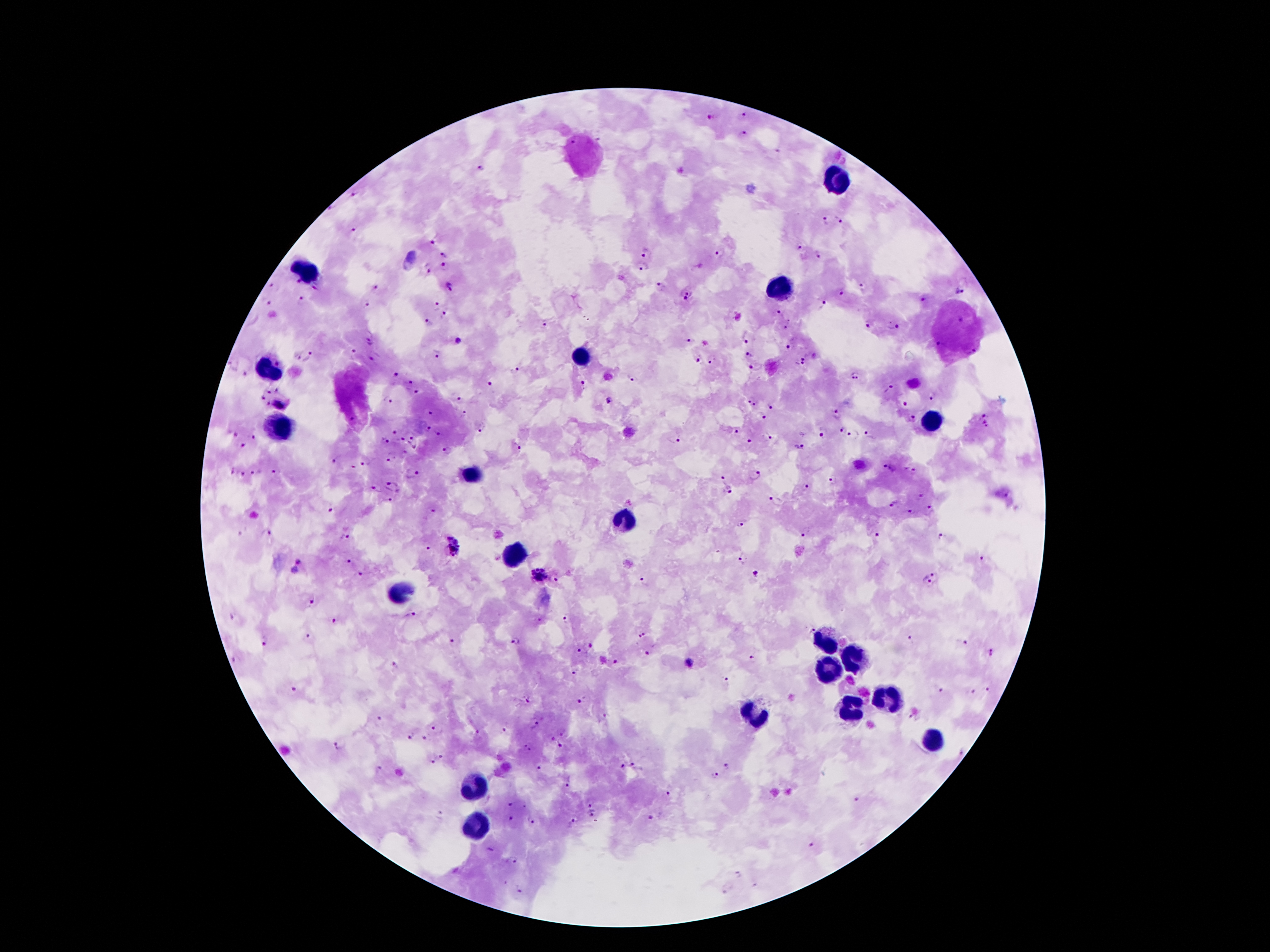

Approximate centers as [x, y] in pixels.
Summary:
  - Malaria parasite locations: [745, 114], [712, 117], [742, 135], [480, 168], [355, 196], [329, 210], [840, 219], [825, 221], [355, 230], [432, 241], [798, 247], [446, 253], [648, 253], [721, 253], [819, 256], [444, 266], [430, 267], [642, 267], [297, 281], [272, 287], [317, 287], [451, 287], [659, 287], [376, 288], [862, 288], [959, 292], [842, 293], [686, 296], [301, 299], [923, 300], [269, 302], [367, 303], [822, 304], [436, 305], [779, 313], [444, 314], [429, 323], [544, 325], [867, 325], [896, 327], [783, 328], [747, 337], [458, 340], [689, 340], [370, 341], [937, 345], [789, 346], [354, 350], [438, 351], [748, 355], [805, 356], [307, 357], [697, 359], [369, 360], [713, 360], [232, 364], [755, 366], [799, 366], [516, 370], [245, 375], [394, 375], [855, 375], [632, 378], [412, 380], [491, 382], [582, 383], [278, 388], [889, 388], [268, 392], [418, 392], [932, 397], [263, 398], [458, 399], [389, 400], [747, 400], [608, 401], [280, 402], [268, 403], [756, 404], [904, 404], [770, 406], [431, 412], [464, 412], [983, 414], [835, 415], [762, 416], [913, 419], [353, 420], [482, 426], [986, 426], [841, 429], [394, 431], [428, 431], [440, 432], [736, 432], [234, 433], [822, 433], [870, 434], [853, 435], [253, 436], [767, 437], [402, 438], [411, 438], [675, 438], [385, 440], [750, 442], [243, 445], [414, 446], [799, 447], [517, 448], [449, 450], [405, 452], [390, 456], [336, 459], [364, 460], [352, 466], [891, 468], [913, 470], [232, 471], [257, 471], [275, 473], [413, 473], [243, 475], [754, 475], [722, 478], [833, 481], [393, 486], [805, 487], [376, 488], [730, 490], [921, 497], [389, 501], [775, 501], [893, 504], [331, 510], [432, 511], [912, 511], [929, 511], [742, 521], [265, 532], [807, 532], [875, 533], [347, 537], [940, 538], [455, 544], [428, 548], [743, 558], [982, 560], [348, 562], [758, 572], [360, 574], [539, 574], [936, 575], [556, 580], [644, 580], [927, 580], [310, 602], [412, 615], [568, 619], [537, 620], [335, 622], [809, 627], [642, 635], [307, 636], [909, 640], [451, 641], [514, 641], [264, 642], [964, 644], [591, 646], [581, 649], [651, 652], [992, 652], [752, 658], [236, 659], [616, 662], [689, 663], [395, 664], [575, 673], [726, 679], [294, 688], [940, 691], [988, 691], [973, 693], [527, 700], [581, 701], [602, 717], [378, 719], [534, 725], [436, 729], [507, 729], [562, 731], [479, 732], [411, 736], [424, 738], [552, 738], [338, 745], [559, 745], [528, 747], [442, 755], [432, 760], [622, 766], [726, 766], [539, 767], [637, 767], [378, 770], [714, 776], [564, 784], [668, 793], [857, 799], [591, 803], [510, 804], [441, 815], [590, 815], [650, 817], [511, 820], [530, 821], [574, 821], [811, 845], [511, 860], [738, 875], [519, 891]
  - Leukocyte locations: [841, 178], [306, 271], [781, 290], [580, 357], [266, 369], [932, 422], [279, 427], [471, 472], [624, 522], [512, 555], [402, 593], [828, 640], [859, 659], [832, 670], [888, 698], [850, 708], [750, 712], [934, 740], [475, 789], [474, 821]
  - Preparation: thick peripheral-blood smear
  - Magnification: 100x
  - Image size: 1270×952 pixels
  - Capture: smartphone through the microscope eyepiece
  - Field of view: one from this slide
  - Stain: Giemsa
  - Patient malaria status: infected with Plasmodium falciparum